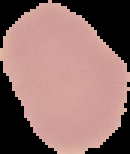

Summary:
  - Preparation: thin blood smear
  - Image size: 130×154 pixels
  - Malaria status: uninfected
  - Image type: segmented cell region on a black background